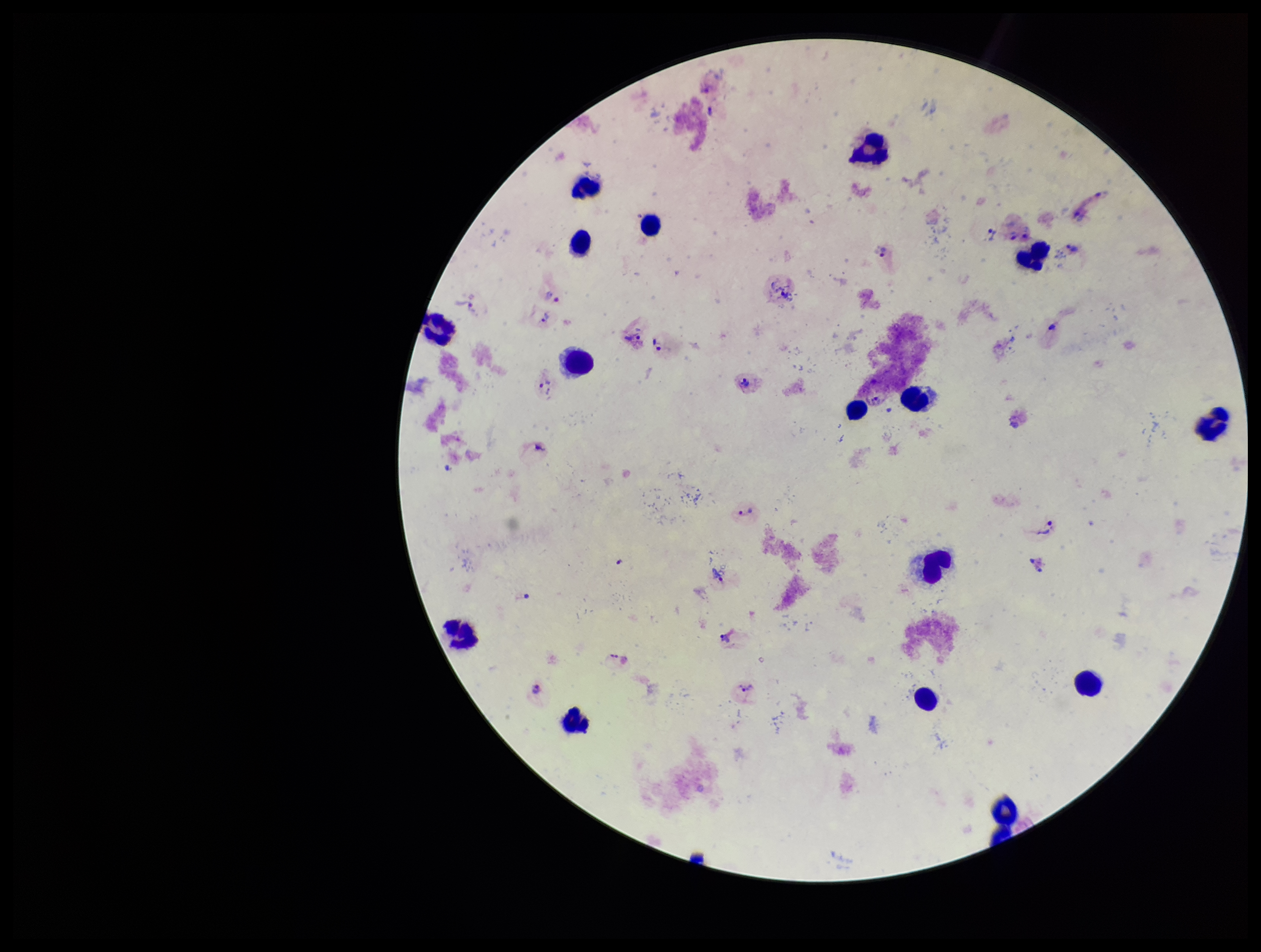
species reported for this patient = Plasmodium vivax
leukocyte count = 16
patient malaria status = infected
Plasmodium parasites = identified
stain = Giemsa
parasite count = 17
preparation = thick smear
field of view = one from this slide
capture = smartphone photograph through the microscope eyepiece
image size = 1261×952 pixels